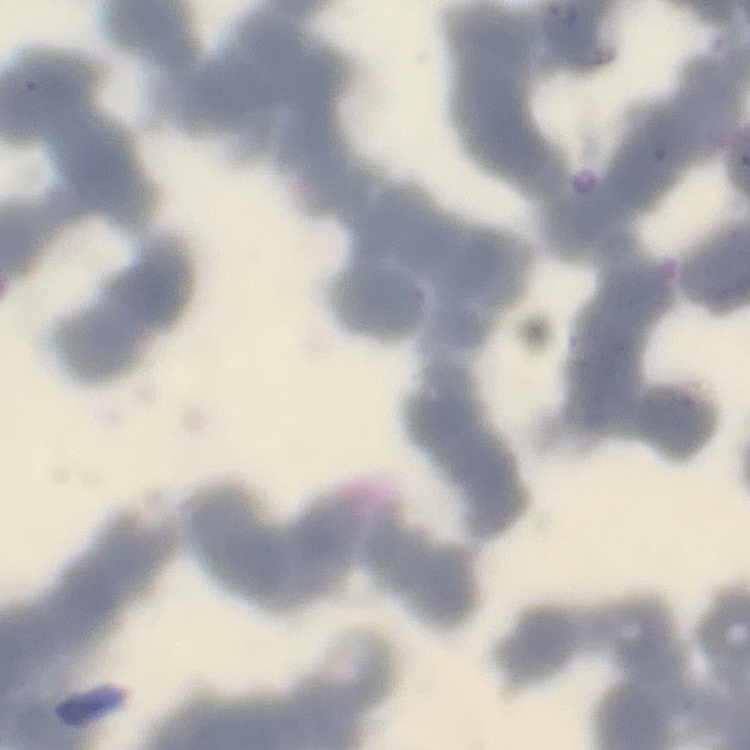 The red blood cells exhibit rouleaux formation. Square crop of a larger photomicrograph. Thin blood smear. Stained with either Field's or Giemsa.